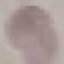

{
  "malaria_status": "uninfected",
  "image_type": "automatically extracted cell patch, resized to 64 × 64 pixels",
  "capture": "smartphone camera at the microscope eyepiece",
  "stain": "Giemsa",
  "preparation": "thin smear"
}